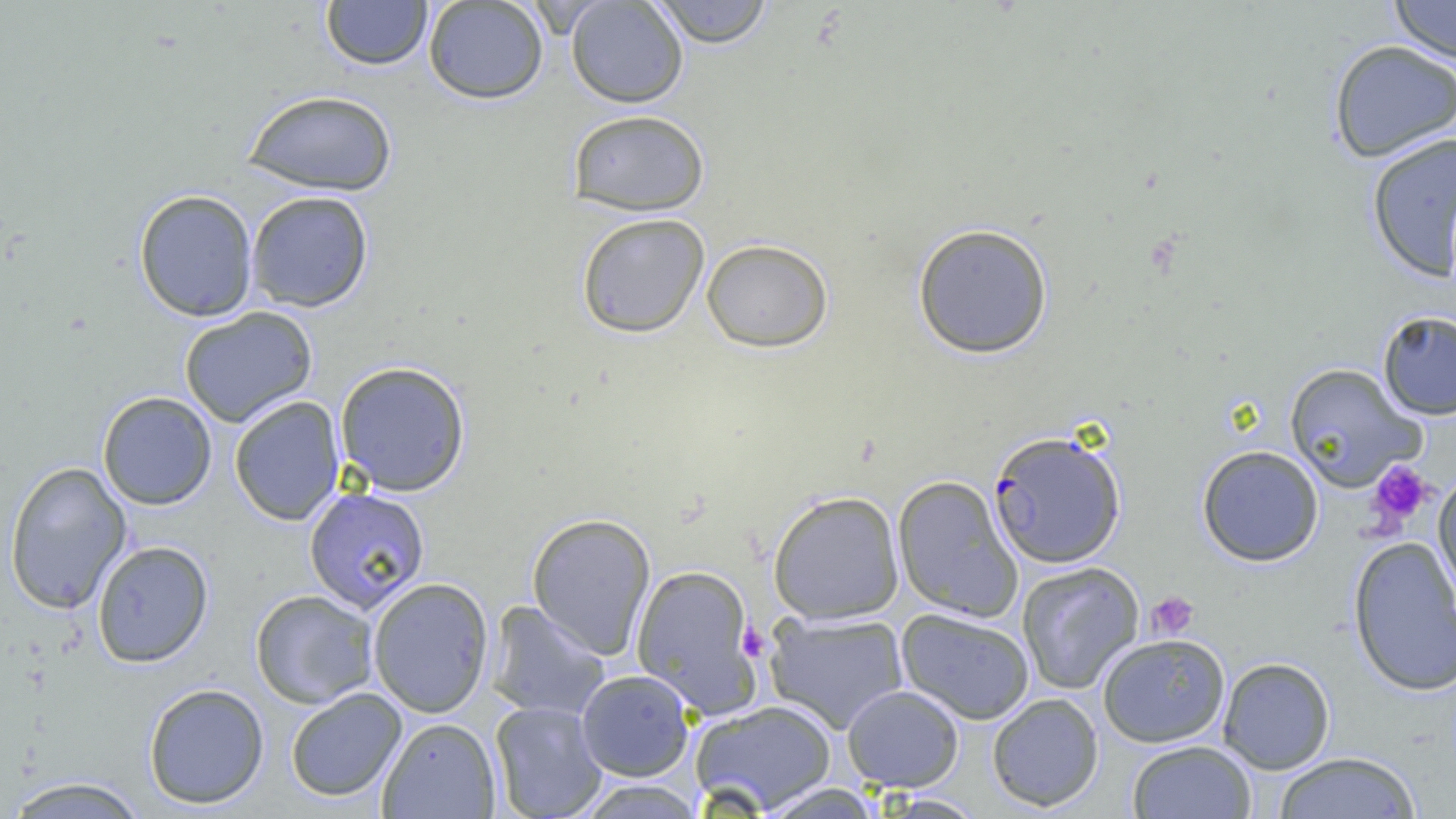

slide-level diagnosis = Plasmodium falciparum
modality = optical microscopy
platelet locations = approximate bounding boxes as named x1/y1/x2/y2 corners in pixels: (x1=1366, y1=460, x2=1435, y2=529), (x1=1146, y1=591, x2=1200, y2=641), (x1=737, y1=622, x2=770, y2=663)
uninfected red blood cell locations = approximate bounding boxes as named x1/y1/x2/y2 corners in pixels: (x1=320, y1=0, x2=433, y2=71), (x1=422, y1=0, x2=549, y2=105), (x1=565, y1=0, x2=688, y2=108), (x1=648, y1=0, x2=775, y2=47), (x1=1389, y1=0, x2=1456, y2=66), (x1=1327, y1=39, x2=1456, y2=162), (x1=242, y1=89, x2=399, y2=197), (x1=567, y1=109, x2=710, y2=215), (x1=1365, y1=132, x2=1456, y2=282), (x1=133, y1=189, x2=259, y2=322), (x1=245, y1=190, x2=374, y2=313), (x1=575, y1=212, x2=711, y2=339), (x1=912, y1=222, x2=1054, y2=359), (x1=701, y1=237, x2=833, y2=353), (x1=179, y1=306, x2=318, y2=428), (x1=1377, y1=310, x2=1456, y2=420), (x1=334, y1=360, x2=471, y2=496), (x1=1284, y1=363, x2=1426, y2=491), (x1=97, y1=391, x2=217, y2=510), (x1=229, y1=396, x2=345, y2=526), (x1=1196, y1=445, x2=1324, y2=567), (x1=4, y1=461, x2=132, y2=614), (x1=1433, y1=468, x2=1456, y2=605), (x1=892, y1=475, x2=1023, y2=623), (x1=303, y1=486, x2=431, y2=614), (x1=767, y1=489, x2=905, y2=625), (x1=527, y1=512, x2=657, y2=660), (x1=1347, y1=535, x2=1456, y2=697), (x1=91, y1=540, x2=214, y2=668), (x1=1016, y1=561, x2=1145, y2=695), (x1=631, y1=564, x2=763, y2=718), (x1=367, y1=577, x2=494, y2=718), (x1=249, y1=589, x2=379, y2=709), (x1=484, y1=601, x2=611, y2=722), (x1=896, y1=608, x2=1035, y2=725), (x1=764, y1=611, x2=909, y2=735), (x1=1097, y1=633, x2=1230, y2=748), (x1=1217, y1=657, x2=1335, y2=774), (x1=576, y1=669, x2=694, y2=781), (x1=143, y1=683, x2=270, y2=809), (x1=842, y1=685, x2=965, y2=792), (x1=285, y1=687, x2=407, y2=802), (x1=987, y1=693, x2=1104, y2=812), (x1=690, y1=700, x2=838, y2=815), (x1=489, y1=701, x2=609, y2=819), (x1=377, y1=717, x2=501, y2=818), (x1=1126, y1=740, x2=1257, y2=818), (x1=1273, y1=751, x2=1421, y2=818), (x1=2, y1=776, x2=151, y2=818), (x1=574, y1=779, x2=706, y2=818), (x1=756, y1=782, x2=884, y2=819), (x1=873, y1=794, x2=988, y2=818)
image size = 1456×819 pixels
field of view = one of a larger specimen
Plasmodium falciparum-infected red blood cell locations = approximate bounding boxes as named x1/y1/x2/y2 corners in pixels: (x1=988, y1=429, x2=1127, y2=569)
magnification = 1000x
preparation = thin blood smear